Identify the parasite.
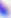

Toxoplasma gondii.

Captured at 400x magnification. Photomicrograph.